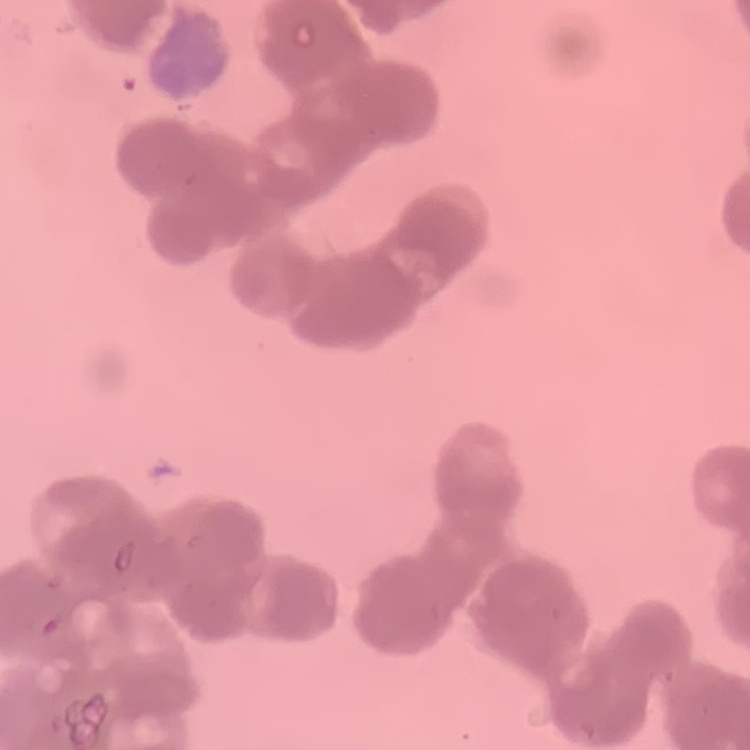
The red blood cells show rouleaux formation. Stained with either Field's or Giemsa. Square crop of a larger photomicrograph. Thin peripheral smear.